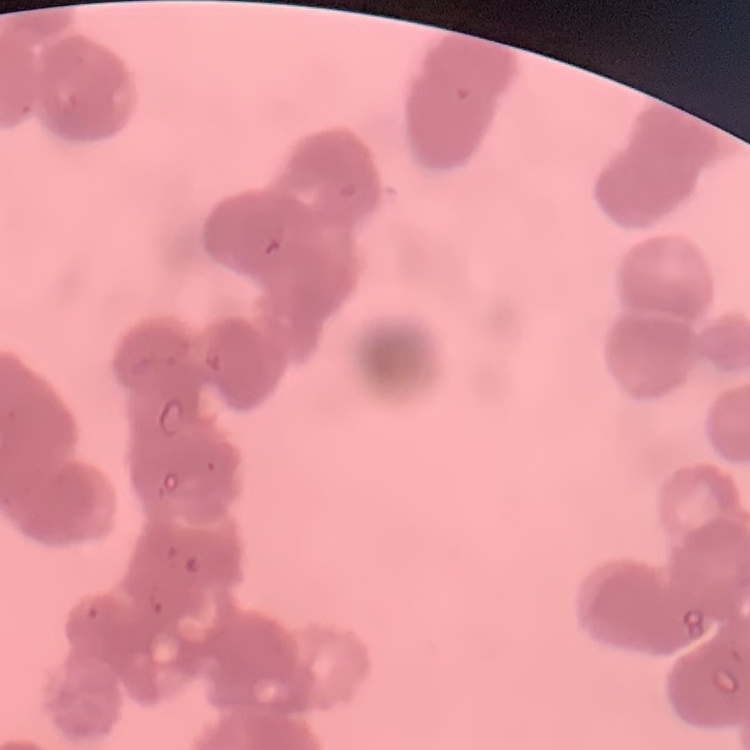

erythrocyte morphology = rouleaux formation
preparation = thin blood smear
stain = Field's or Giemsa
image type = one tile cut from a larger photomicrograph